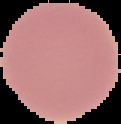
preparation = thin blood film
malaria status = uninfected
image size = 121×124 pixels
image type = segmented cell region on a black background